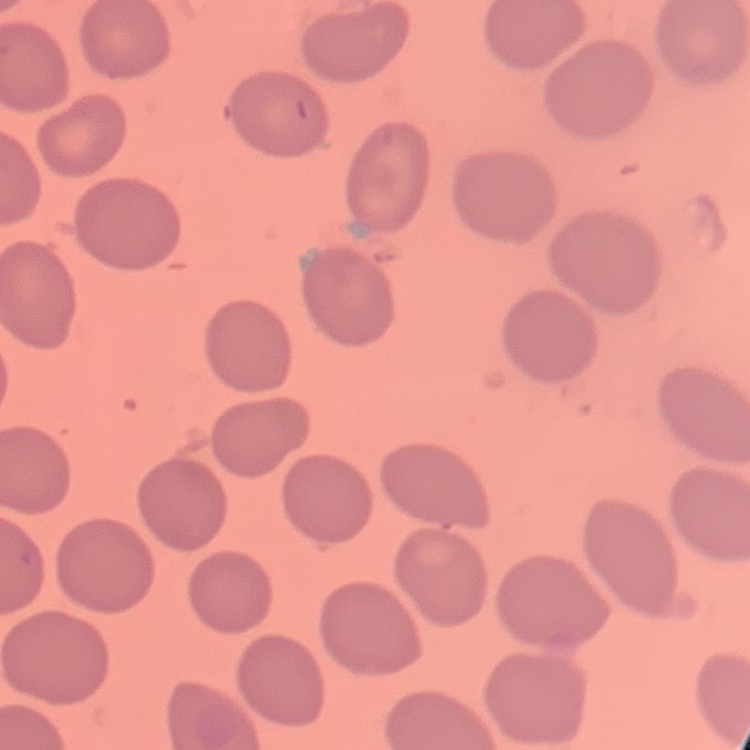

The erythrocytes exhibit no rouleaux formation. Stained with either Field's or Giemsa. Square crop of a larger photomicrograph. Thin blood film.